Give the preparation type.
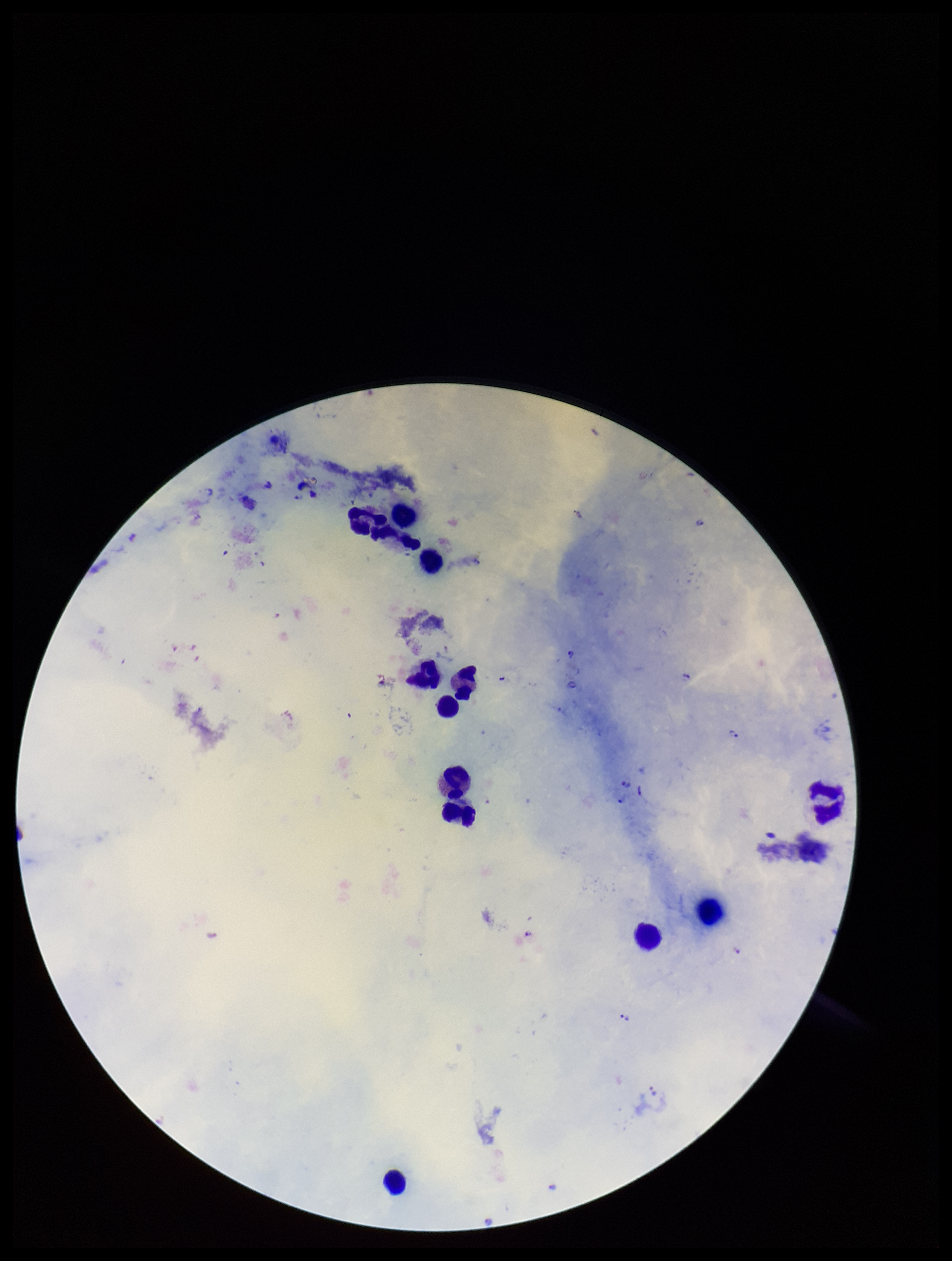
Thick.

Parasite count: 11. Image is 952×1261 pixels. Species reported for this patient: Plasmodium falciparum. Plasmodium parasites: seen. Photographed through the microscope eyepiece with a smartphone camera. Leukocyte count: 12. Stained with Giemsa. One field from this slide. Patient malaria status: infected.